Assess this cell for malaria.
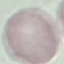
Uninfected.

preparation = thin blood film
capture = smartphone camera at the microscope eyepiece
stain = Giemsa
image type = cell patch, automatically extracted from a larger field of view and resized to 64 × 64 pixels